Outline each blood parasite and name the species.
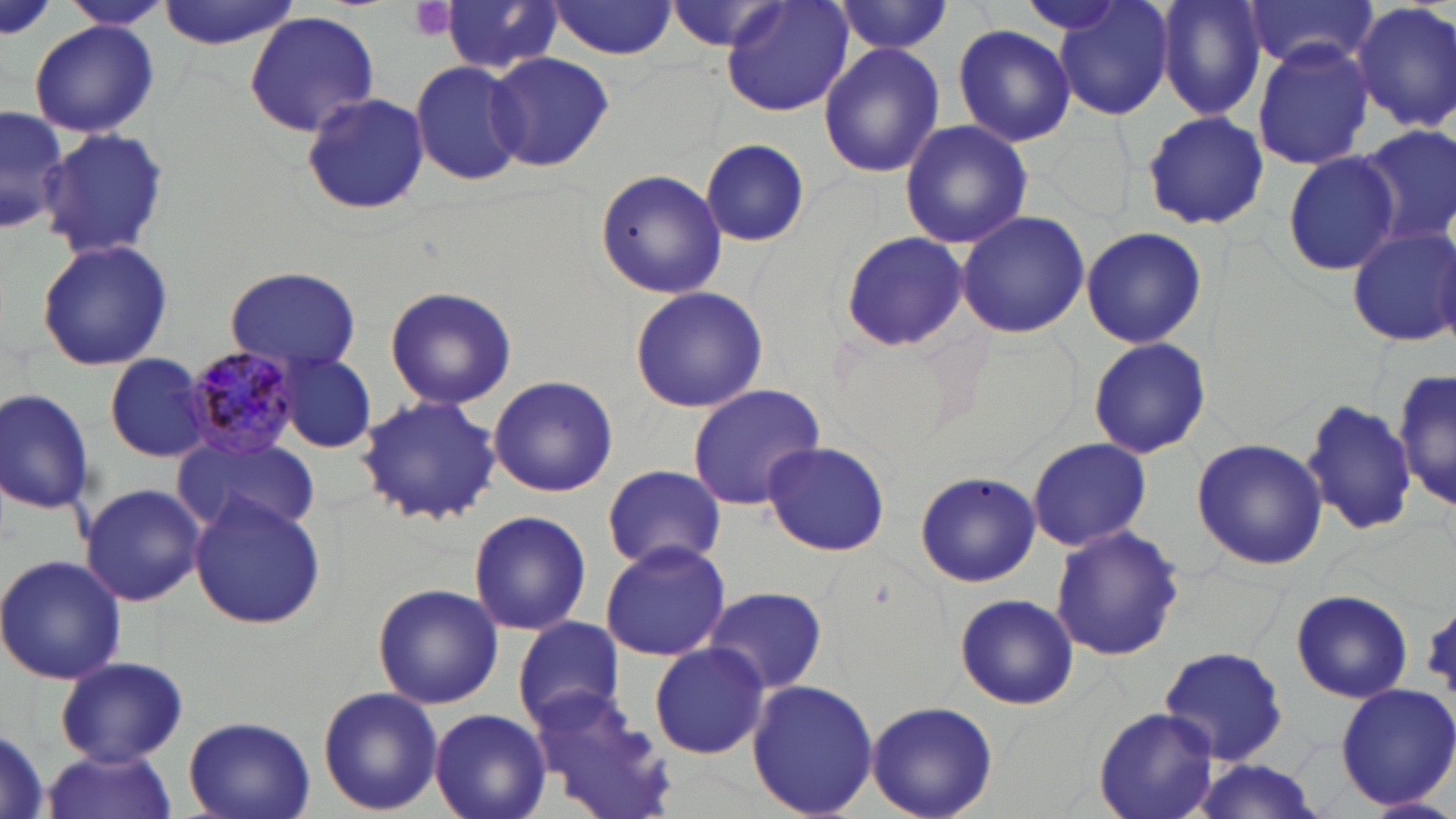

Approximate bounding boxes as (x1, y1, x2, y2) in pixels.
Plasmodium malariae-infected red blood cells: (182, 346, 303, 458).
No Plasmodium falciparum, Plasmodium ovale, Plasmodium vivax, Babesia divergens, or Trypanosoma brucei observed.

Summary:
  - Uninfected red blood cell locations: (0, 0, 56, 45), (66, 0, 168, 29), (156, 0, 301, 49), (722, 0, 854, 118), (1051, 0, 1176, 121), (1155, 0, 1266, 120), (1243, 0, 1379, 75), (550, 1, 678, 59), (441, 2, 562, 77), (831, 2, 953, 57), (1351, 2, 1456, 133), (244, 10, 381, 138), (29, 20, 157, 138), (951, 23, 1079, 146), (1251, 39, 1376, 171), (818, 43, 947, 178), (487, 52, 616, 172), (410, 59, 526, 188), (300, 94, 429, 215), (1, 101, 66, 237), (1141, 109, 1271, 232), (899, 119, 1033, 249), (1355, 125, 1456, 251), (38, 128, 171, 262), (700, 139, 809, 246), (1280, 152, 1398, 277), (595, 170, 728, 300), (955, 210, 1090, 340), (1080, 225, 1207, 350), (1345, 225, 1456, 348), (839, 234, 970, 350), (36, 239, 172, 372), (223, 265, 365, 372), (382, 284, 518, 410), (630, 286, 768, 413), (1086, 337, 1213, 459), (277, 351, 376, 452), (104, 352, 212, 461), (1392, 364, 1454, 515), (487, 375, 619, 498), (685, 383, 825, 511), (0, 387, 95, 514), (356, 394, 505, 524), (1302, 398, 1419, 539), (174, 434, 319, 537), (1027, 437, 1153, 551), (1191, 438, 1328, 570), (762, 441, 891, 558), (600, 464, 726, 570), (912, 471, 1037, 587), (80, 482, 206, 607), (189, 494, 326, 630), (468, 509, 591, 636), (1050, 526, 1184, 662), (599, 539, 732, 661), (0, 553, 126, 685), (373, 582, 504, 710), (702, 584, 829, 695), (1290, 588, 1413, 703), (956, 593, 1079, 711), (1423, 610, 1456, 691), (510, 616, 627, 732), (648, 643, 771, 759), (1159, 645, 1293, 768), (1160, 646, 1288, 765), (55, 656, 190, 766), (745, 678, 879, 819), (1332, 681, 1456, 811), (525, 684, 683, 819), (317, 686, 444, 815), (866, 700, 998, 819), (429, 708, 552, 819), (1094, 708, 1219, 819), (182, 715, 316, 819), (0, 722, 49, 819), (40, 751, 179, 819), (1178, 762, 1334, 819), (1364, 794, 1455, 819)
  - Platelet locations: (409, 0, 457, 41)
  - Slide-level diagnosis: Plasmodium malariae
  - Modality: optical microscopy
  - Preparation: thin blood film
  - Field of view: one of a larger specimen
  - Image size: 1456×819 pixels
  - Stain: May-Grünwald-Giemsa
  - Magnification: 1000x